Evaluate for malaria.
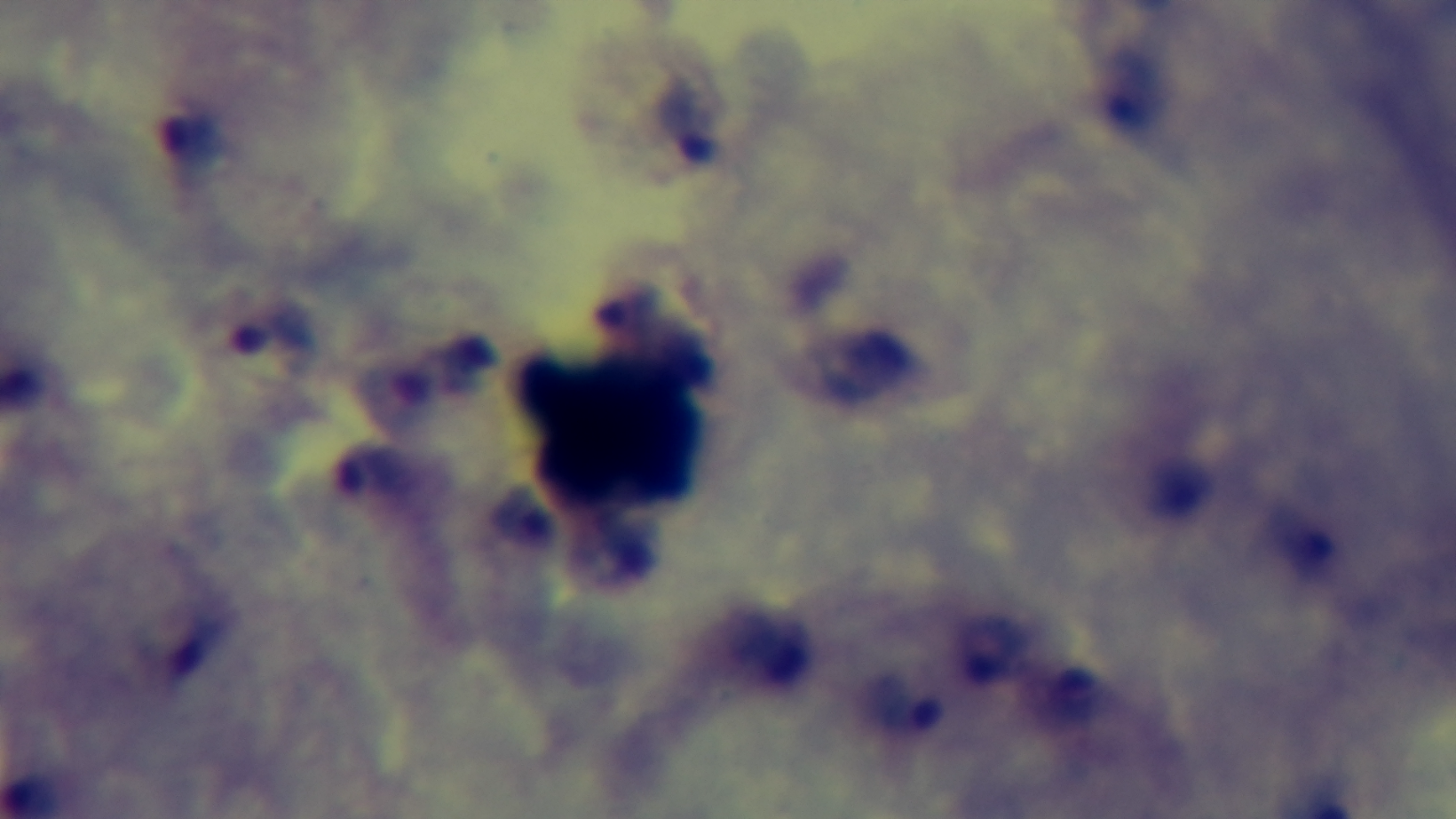
Positive.

Giemsa stain. 100x oil-immersion objective. Captured with a mounted 4K digital camera. Single field of view. Photomicrograph. Preparation: thick blood film.